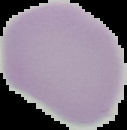 Image is 127×130 pixels. From a thin blood film. Segmented cell region on a black background. Result: no Plasmodium parasites detected.